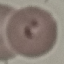
result: malaria parasites detected
capture: smartphone through the microscope eyepiece
image_type: cell patch, automatically extracted from a larger field of view and resized to 64 × 64 pixels
stain: Giemsa
preparation: thin blood film